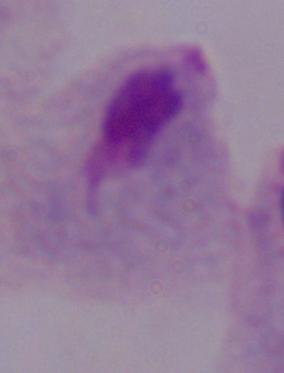
Summary:
  - Magnification: 1000x
  - Modality: photomicrograph
  - Identification: trichomonad